Outline each blood parasite and name the species.
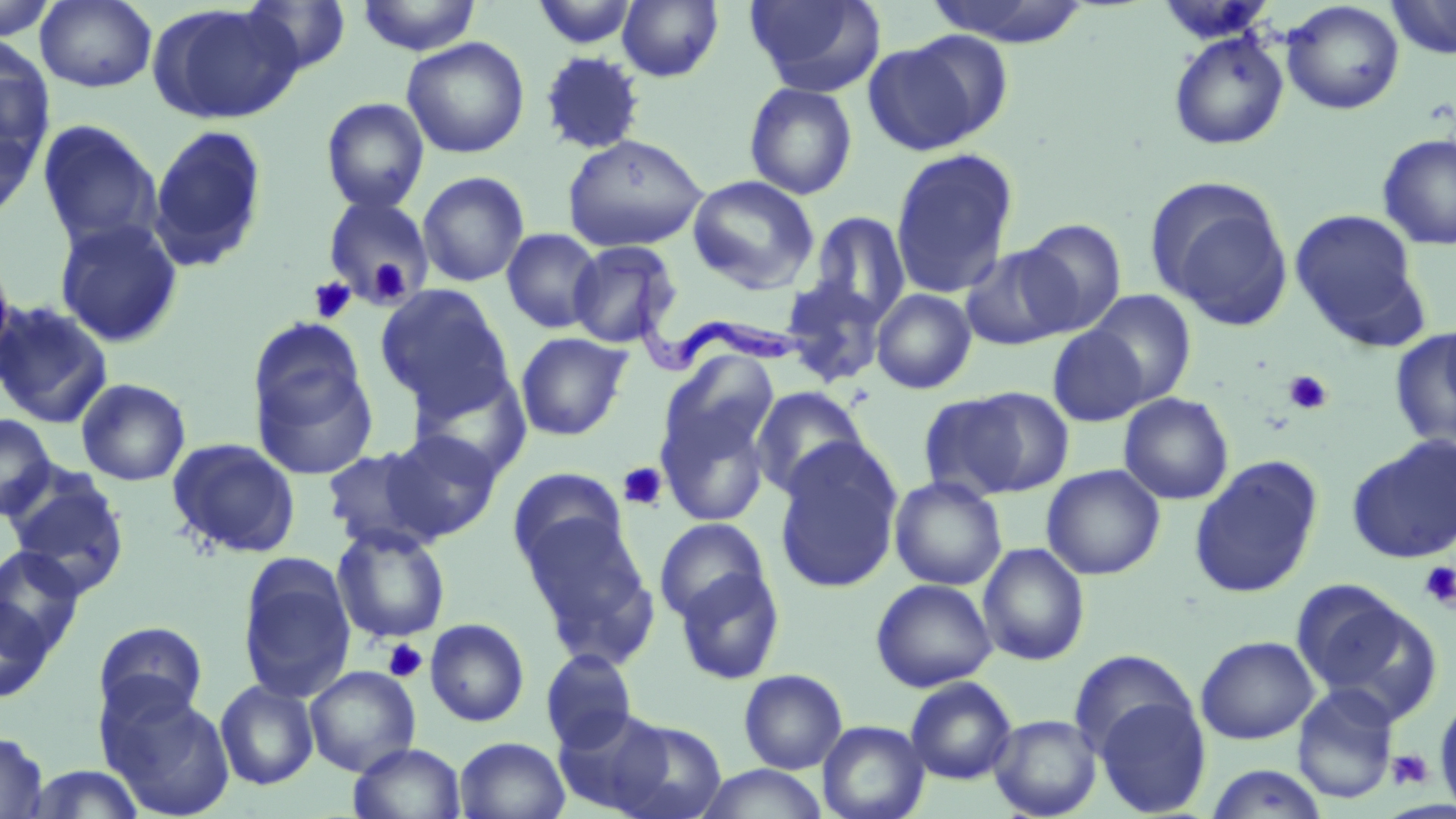
Approximate bounding boxes as (x1, y1, x2, y2) in pixels.
Trypanosoma brucei: (608, 259, 806, 379).
No Plasmodium falciparum, Plasmodium ovale, Plasmodium malariae, Plasmodium vivax, or Babesia divergens observed.

Uninfected red blood cell locations: (0, 0, 60, 41), (35, 0, 157, 93), (241, 0, 352, 76), (356, 0, 482, 56), (531, 0, 640, 50), (617, 0, 723, 82), (744, 0, 885, 96), (923, 0, 1091, 46), (1386, 0, 1456, 59), (1155, 2, 1276, 46), (1281, 2, 1405, 115), (148, 4, 301, 125), (900, 30, 1016, 142), (1168, 31, 1290, 151), (0, 34, 55, 167), (401, 36, 530, 159), (539, 51, 646, 155), (743, 82, 858, 200), (320, 97, 430, 214), (0, 117, 41, 222), (38, 120, 162, 251), (146, 124, 269, 273), (1377, 133, 1456, 250), (562, 134, 709, 252), (889, 148, 1019, 300), (416, 171, 530, 288), (686, 175, 819, 293), (1148, 178, 1294, 328), (320, 196, 437, 304), (1290, 210, 1424, 344), (806, 211, 911, 326), (54, 217, 183, 348), (1019, 218, 1127, 335), (501, 228, 604, 333), (0, 240, 18, 387), (567, 240, 681, 347), (959, 245, 1076, 351), (779, 278, 889, 387), (373, 285, 513, 414), (871, 288, 976, 394), (1085, 290, 1197, 405), (0, 301, 114, 429), (1439, 317, 1456, 418), (1047, 326, 1150, 427), (1389, 330, 1456, 451), (515, 332, 632, 441), (249, 350, 379, 481), (658, 352, 779, 470), (409, 369, 531, 481), (76, 378, 191, 486), (750, 385, 871, 500), (927, 386, 1075, 500), (1118, 393, 1234, 505), (654, 397, 775, 528), (0, 413, 57, 522), (382, 429, 503, 542), (1347, 436, 1456, 564), (167, 438, 301, 559), (773, 440, 904, 595), (321, 445, 445, 553), (1188, 457, 1323, 600), (1042, 464, 1165, 580), (507, 467, 631, 575), (889, 476, 1008, 591), (6, 477, 130, 599), (521, 513, 656, 662), (654, 517, 770, 624), (332, 524, 450, 644), (977, 542, 1090, 666), (0, 547, 85, 656), (238, 560, 356, 702), (674, 566, 786, 685), (870, 578, 997, 692), (1294, 582, 1437, 721), (0, 596, 55, 704), (424, 617, 530, 727), (93, 622, 209, 724), (1195, 635, 1319, 744), (1069, 649, 1196, 760), (541, 650, 638, 753), (304, 666, 421, 776), (738, 669, 848, 774), (905, 676, 1017, 784), (214, 680, 319, 790), (1292, 684, 1399, 804), (99, 685, 236, 819), (1094, 696, 1212, 816), (1434, 696, 1456, 815), (553, 708, 675, 815), (988, 713, 1103, 819), (608, 718, 727, 819), (817, 720, 929, 819), (0, 731, 48, 818), (454, 736, 570, 819), (348, 742, 466, 819), (23, 764, 146, 819), (697, 764, 827, 819), (1204, 764, 1329, 819). Platelet locations: (366, 257, 412, 306), (309, 277, 356, 324), (1284, 370, 1333, 414), (618, 462, 669, 510), (1418, 561, 1456, 609), (383, 639, 427, 683), (1387, 748, 1433, 789). Slide-level diagnosis: Trypanosoma brucei. Thin blood film. Light microscopy. Image is 1456×819 pixels. 1000x magnification. One field of a larger specimen. May-Grünwald-Giemsa-stained preparation.